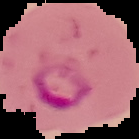

Segmented cell region on a black background. Image is 139×139 pixels. From a thin blood smear. Result: Plasmodium parasites detected.